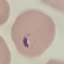
Summary:
  - Result: malaria parasites detected
  - Stain: Giemsa
  - Preparation: thin blood smear
  - Image type: cell patch, automatically extracted from a larger field of view and resized to 64 × 64 pixels
  - Capture: smartphone through the microscope eyepiece